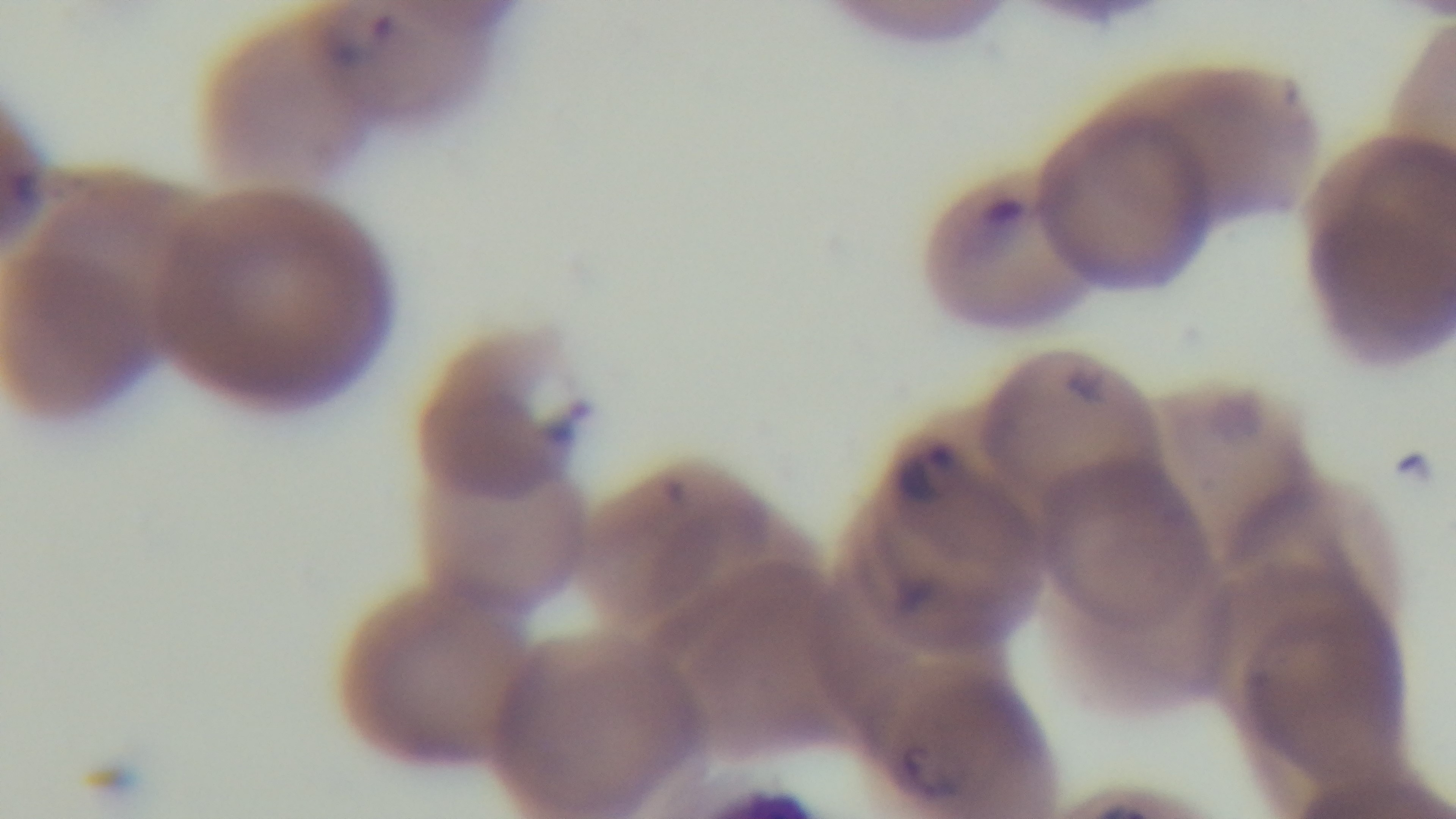

Giemsa-stained. Captured with a mounted 4K digital camera. Preparation: thin smear. One field from the slide. 100x oil-immersion objective. Photomicrograph. Malaria status: positive.